State which cell type is depicted.
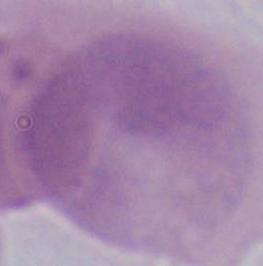
This is an erythrocyte.

Summary:
  - Magnification: 1000x
  - Modality: micrograph